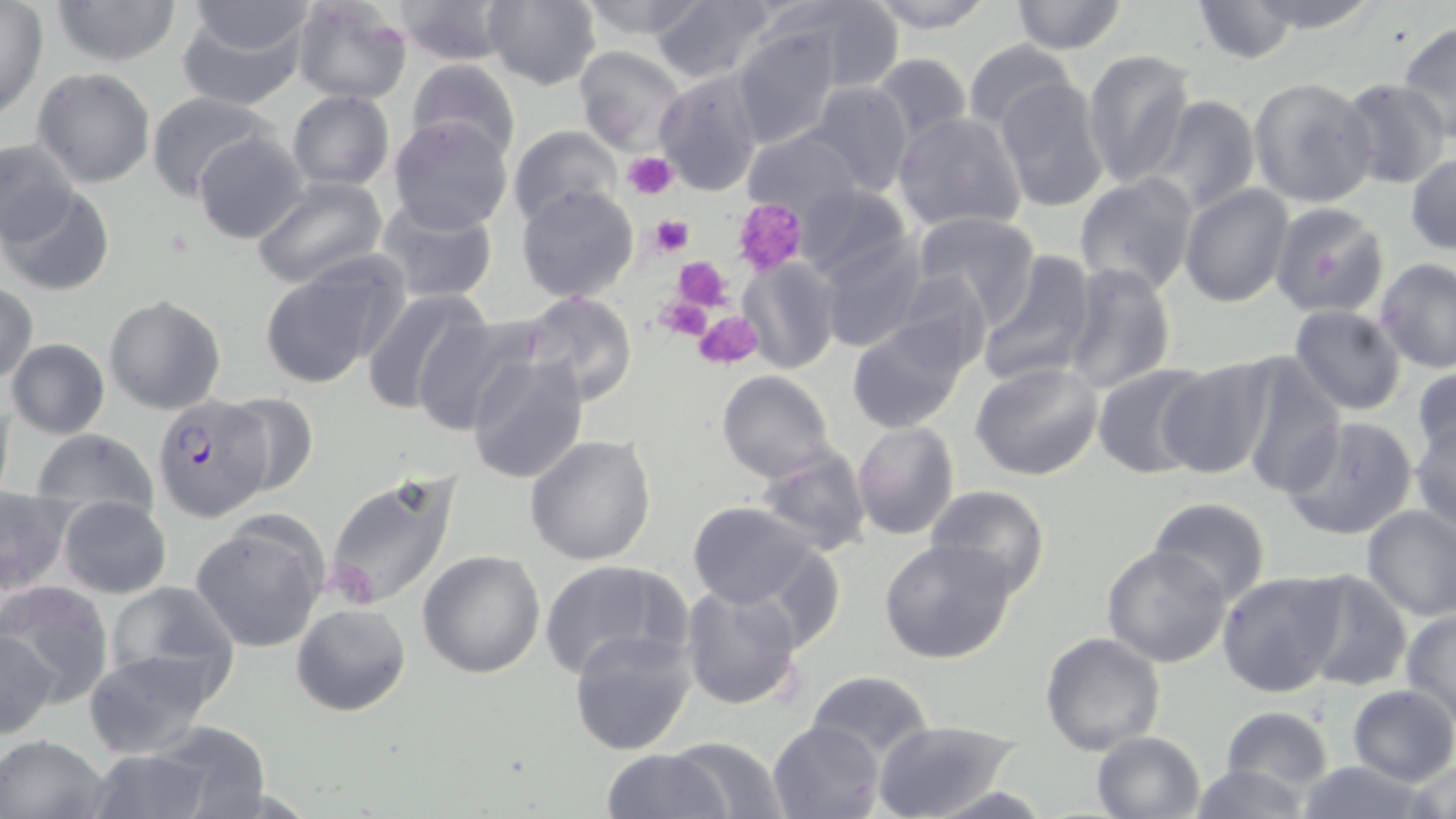

Plasmodium falciparum-infected red blood cell locations = approximate bounding boxes as [x1, y1, x2, y2] in pixels: [152, 394, 272, 522]
slide-level diagnosis = Plasmodium falciparum
preparation = thin blood film
field of view = single
stain = May-Grünwald-Giemsa
magnification = 1000x
modality = optical microscopy
image size = 1456×819 pixels
platelet locations = approximate bounding boxes as [x1, y1, x2, y2] in pixels: [622, 151, 679, 201], [732, 197, 809, 276], [647, 216, 695, 262], [673, 256, 732, 307], [654, 298, 713, 342], [694, 310, 764, 369]
uninfected red blood cell locations = approximate bounding boxes as [x1, y1, x2, y2] in pixels: [50, 0, 183, 68], [292, 0, 413, 105], [394, 0, 514, 65], [482, 0, 600, 91], [576, 0, 709, 42], [651, 0, 778, 84], [767, 0, 902, 92], [862, 0, 998, 32], [1009, 0, 1127, 54], [1190, 0, 1302, 64], [1242, 0, 1383, 33], [179, 1, 312, 109], [0, 2, 48, 120], [1397, 19, 1456, 140], [732, 29, 840, 149], [962, 39, 1080, 137], [572, 45, 689, 157], [1080, 48, 1197, 189], [869, 54, 971, 146], [406, 57, 521, 162], [32, 67, 158, 188], [653, 70, 764, 196], [1248, 75, 1379, 211], [993, 77, 1109, 213], [1335, 79, 1452, 189], [806, 81, 912, 198], [146, 90, 276, 201], [287, 90, 394, 191], [1139, 92, 1263, 215], [892, 110, 1027, 234], [387, 116, 515, 235], [508, 124, 620, 226], [740, 128, 863, 218], [192, 131, 310, 245], [0, 138, 79, 249], [1406, 152, 1456, 256], [1074, 172, 1199, 295], [249, 176, 389, 291], [790, 182, 913, 285], [1179, 184, 1294, 307], [2, 185, 114, 298], [516, 185, 639, 302], [372, 196, 500, 307], [1268, 201, 1390, 319], [908, 211, 1042, 324], [817, 234, 927, 353], [977, 252, 1097, 385], [737, 256, 839, 374], [256, 257, 405, 388], [1375, 258, 1456, 373], [1059, 263, 1176, 394], [885, 271, 993, 375], [0, 281, 38, 385], [360, 287, 492, 416], [517, 293, 638, 409], [104, 294, 226, 415], [1288, 305, 1408, 417], [409, 315, 541, 436], [849, 315, 972, 433], [6, 338, 109, 438], [1233, 350, 1346, 498], [465, 353, 590, 484], [1156, 356, 1277, 479], [972, 361, 1104, 480], [1090, 363, 1217, 479], [1411, 364, 1456, 466], [716, 371, 834, 484], [0, 384, 16, 502], [214, 393, 320, 497], [1411, 406, 1456, 534], [1280, 415, 1418, 541], [852, 421, 959, 540], [30, 429, 155, 523], [525, 434, 657, 566], [753, 448, 871, 557], [320, 473, 464, 612], [924, 485, 1051, 599], [0, 487, 73, 598], [59, 496, 171, 598], [1147, 498, 1271, 605], [684, 501, 823, 613], [1360, 504, 1456, 621], [188, 514, 330, 653], [879, 538, 1020, 664], [1102, 544, 1233, 668], [418, 551, 546, 678], [539, 558, 692, 681], [1293, 569, 1415, 691], [1216, 570, 1347, 696], [101, 580, 238, 696], [3, 581, 113, 703], [679, 584, 804, 712], [291, 603, 410, 717], [1401, 611, 1456, 723], [568, 627, 697, 755], [1, 629, 60, 739], [1040, 632, 1165, 752], [80, 648, 224, 760], [805, 670, 934, 760], [1347, 685, 1456, 787], [1219, 706, 1335, 794], [873, 718, 1021, 819], [767, 719, 884, 818], [138, 722, 275, 816], [1092, 730, 1204, 817], [0, 732, 111, 819], [663, 735, 788, 818], [79, 746, 222, 819], [602, 748, 729, 818], [1405, 757, 1456, 819], [1294, 758, 1431, 818], [1187, 763, 1314, 819]